Assess this cell for malaria.
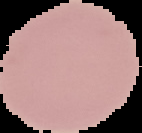

Uninfected.

{
  "preparation": "thin blood smear",
  "image_size": "142×133 pixels",
  "image_type": "segmented cell region on a black background"
}